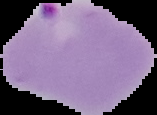

{
  "image_size": "157×115 pixels",
  "result": "malaria parasites identified",
  "preparation": "thin blood film",
  "image_type": "segmented cell region on a black background"
}